Locate and identify every blood parasite.
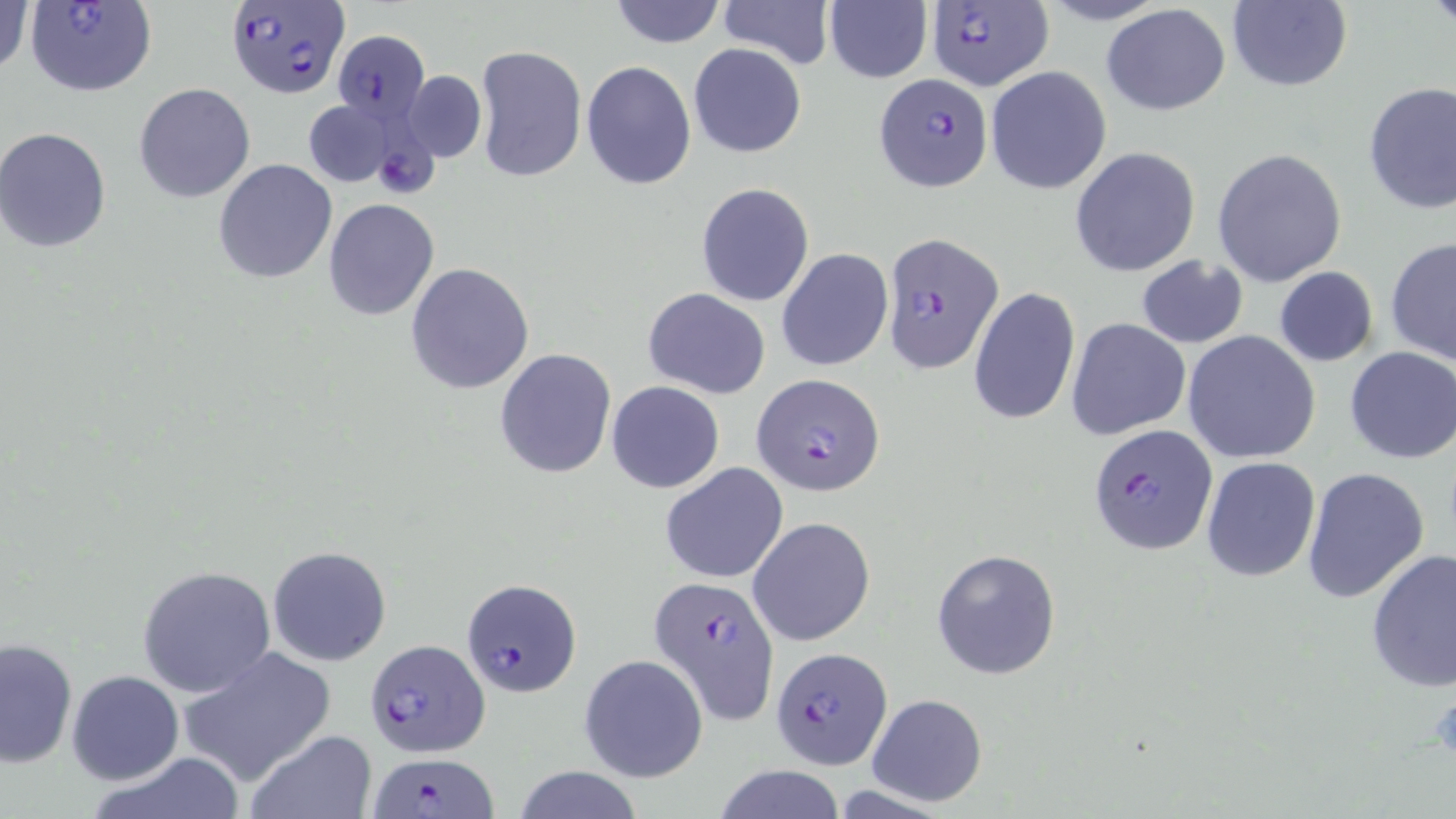
Approximate bounding boxes as (x1,y1)-(x2,y2) corner pairs in pixels.
Plasmodium falciparum-infected red blood cells: (23,0)-(158,97), (225,0)-(348,100), (923,1)-(1055,93), (332,30)-(430,124), (874,74)-(992,192), (879,232)-(1005,372), (751,373)-(885,496), (1088,425)-(1217,555), (651,574)-(778,726), (461,577)-(581,695), (364,635)-(492,753), (772,649)-(892,770), (367,751)-(500,818).
No Plasmodium ovale, Plasmodium malariae, Plasmodium vivax, Babesia divergens, or Trypanosoma brucei observed.

slide_level_diagnosis: Plasmodium falciparum
uninfected_red_blood_cell_locations: 'approximate bounding boxes as (x1,y1)-(x2,y2) corner pairs in pixels: (1,0)-(33,81), (609,0)-(727,49), (716,0)-(835,70), (824,0)-(933,84), (1225,1)-(1352,92), (1101,3)-(1231,116), (688,43)-(807,159), (474,45)-(587,183), (580,60)-(698,190), (985,66)-(1112,194), (403,70)-(486,161), (1362,81)-(1456,214), (135,83)-(255,202), (303,99)-(399,187), (0,129)-(111,252), (1069,146)-(1201,277), (1212,148)-(1348,286), (213,158)-(338,284), (696,183)-(815,305), (322,200)-(440,320), (1385,237)-(1456,370), (776,248)-(892,372), (1135,256)-(1250,349), (405,262)-(534,396), (1273,266)-(1379,367), (643,287)-(770,398), (968,287)-(1080,427), (1066,318)-(1192,441), (1182,330)-(1321,465), (1343,347)-(1456,464), (494,348)-(617,480), (607,380)-(724,493), (1200,456)-(1321,582), (661,463)-(788,583), (1301,467)-(1431,604), (747,516)-(876,647), (267,546)-(392,667), (1365,548)-(1456,692), (930,549)-(1062,680), (135,565)-(278,698), (0,637)-(78,769), (178,645)-(336,786), (579,655)-(708,783), (66,671)-(183,784), (865,693)-(987,807), (245,730)-(376,818), (91,752)-(248,819), (713,764)-(847,819), (510,766)-(646,819)'
preparation: thin blood smear
modality: optical microscopy
stain: May-Grünwald-Giemsa
platelet_locations: 'approximate bounding boxes as (x1,y1)-(x2,y2) corner pairs in pixels: (1426,692)-(1456,766)'
image_size: 1456×819 pixels
field_of_view: one of a larger specimen
magnification: 1000x